Locate every Plasmodium parasite.
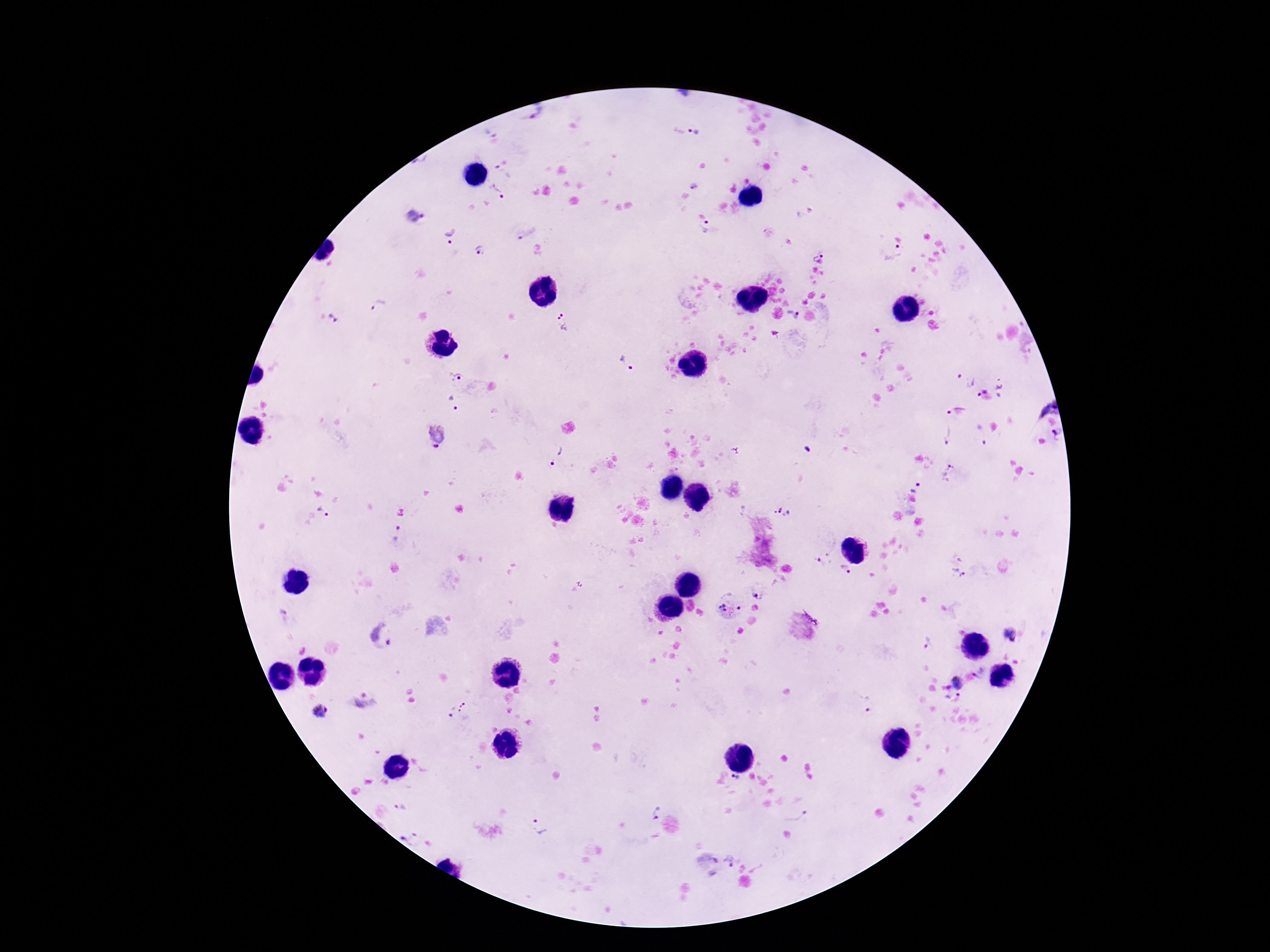
Approximate centers as (x, y) in pixels.
Plasmodium parasites: (540, 114), (491, 130), (694, 132), (498, 191), (415, 217), (707, 228), (526, 229), (450, 237), (482, 249), (817, 253), (895, 254), (379, 306), (793, 315), (335, 318), (564, 324), (627, 364), (456, 378), (965, 380), (1002, 386), (979, 392), (1048, 405), (453, 406), (958, 409), (1057, 432), (947, 433), (981, 433), (435, 436), (807, 450), (736, 451), (556, 455), (947, 469), (915, 487), (783, 511), (324, 512), (397, 533), (825, 558), (845, 570), (958, 574), (758, 594), (722, 607), (740, 608), (383, 634), (1010, 635), (925, 640), (957, 681), (952, 696), (869, 704), (454, 707), (319, 711), (736, 780), (401, 808), (657, 813), (798, 818), (540, 829), (412, 839), (730, 860).

patient malaria status = infected
preparation = thick peripheral-blood smear
stain = Giemsa
image size = 1270×952 pixels
field of view = one from this slide
magnification = 100x
capture = smartphone camera through the microscope eyepiece